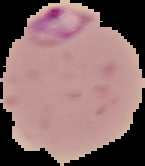

image type = segmented cell region on a black background
preparation = thin blood film
image size = 145×166 pixels
result = Plasmodium parasites detected